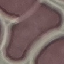 Result: no malaria parasites seen. Photographed with a smartphone camera at the microscope eyepiece. Automatically extracted cell patch, resized to 64 × 64 pixels. Thin blood smear. Giemsa stain.